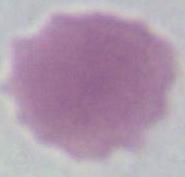 1000x magnification. A red blood cell is seen. Photomicrograph.